Report the malaria status of this cell.
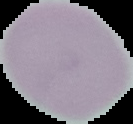

Uninfected.

Summary:
  - Preparation: thin blood smear
  - Image type: segmented cell region on a black background
  - Image size: 133×124 pixels